Point out each malaria parasite.
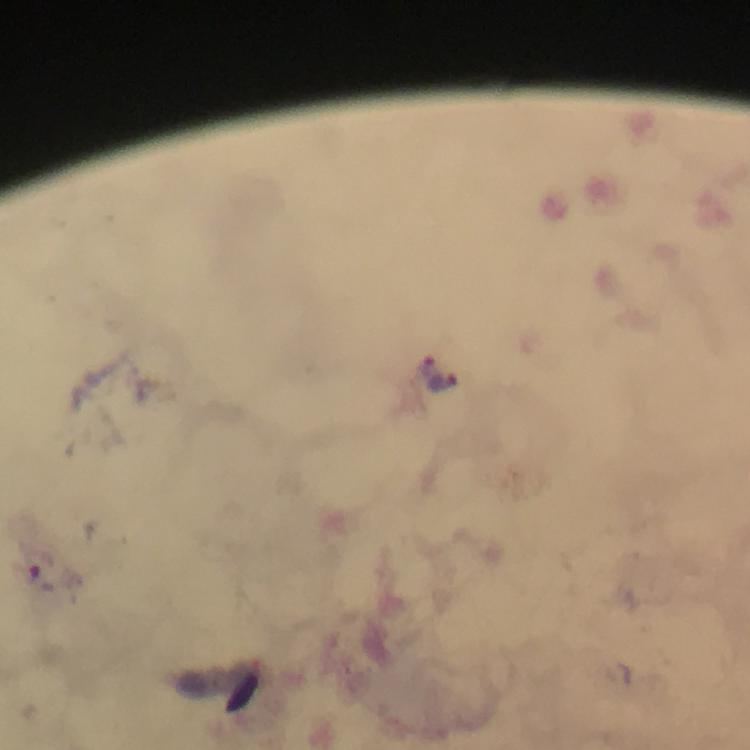

Approximate centers as [x, y] in pixels.
Malaria parasites: [428, 364], [443, 382].

Summary:
  - Cropped from: one field of view
  - Preparation: thick blood smear
  - Magnification: 100x
  - Stain: Giemsa
  - Immersion oil: applied
  - Context: from a diagnostic examination for malaria
  - Image size: 750×750 pixels
  - Capture: smartphone mounted on the microscope